Give the position of every Plasmodium parasite.
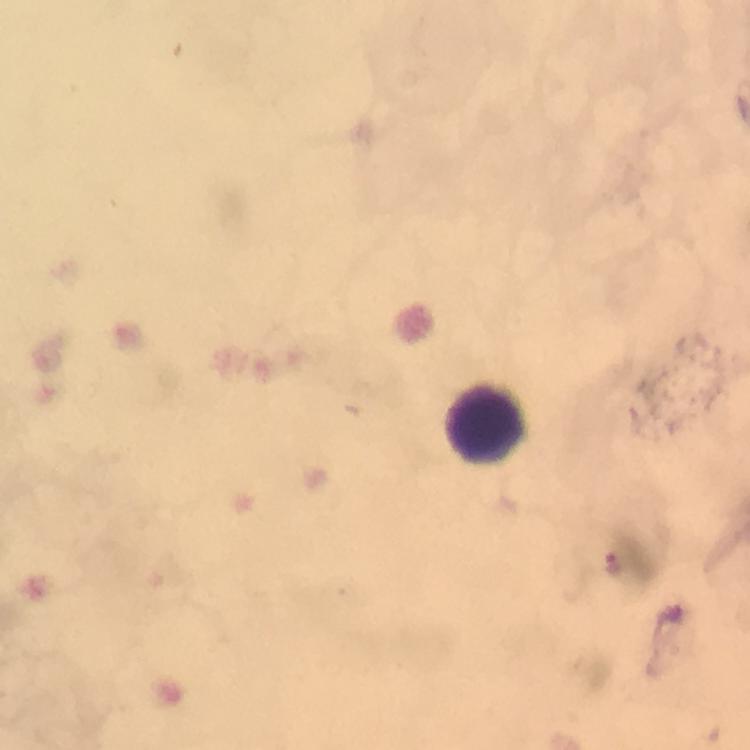

Approximate centers as (x, y) in pixels.
Plasmodium parasites: (614, 563).

Summary:
  - Leukocyte locations: (487, 419)
  - Immersion oil: applied
  - Image size: 750×750 pixels
  - Magnification: 100x
  - Context: from a diagnostic examination for malaria
  - Capture: smartphone photograph through a microscope
  - Cropped from: a single field of view
  - Preparation: thick blood smear
  - Stain: Giemsa